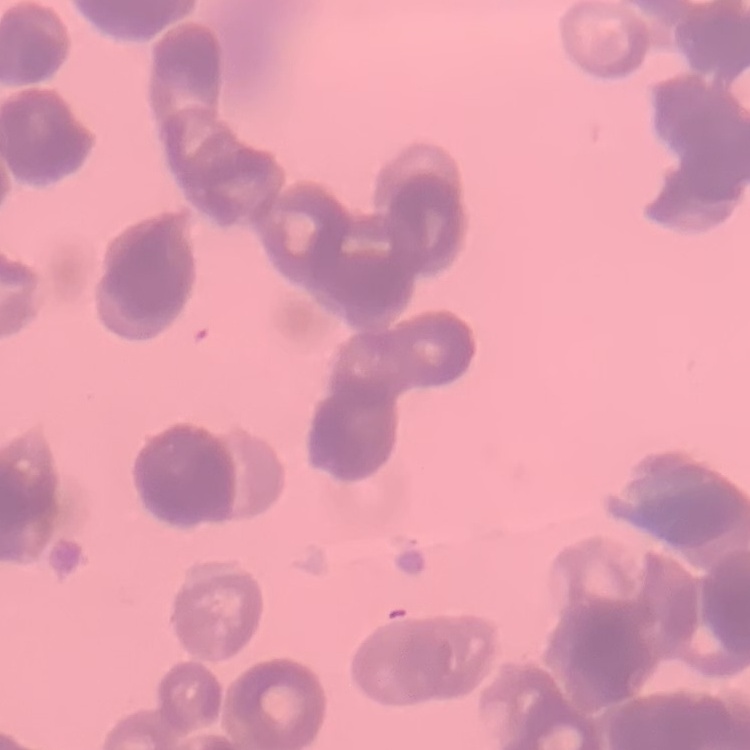
The erythrocytes show rouleaux formation. Thin blood smear. One tile cut from a larger photomicrograph. Field's or Giemsa stain.